Assess for malaria.
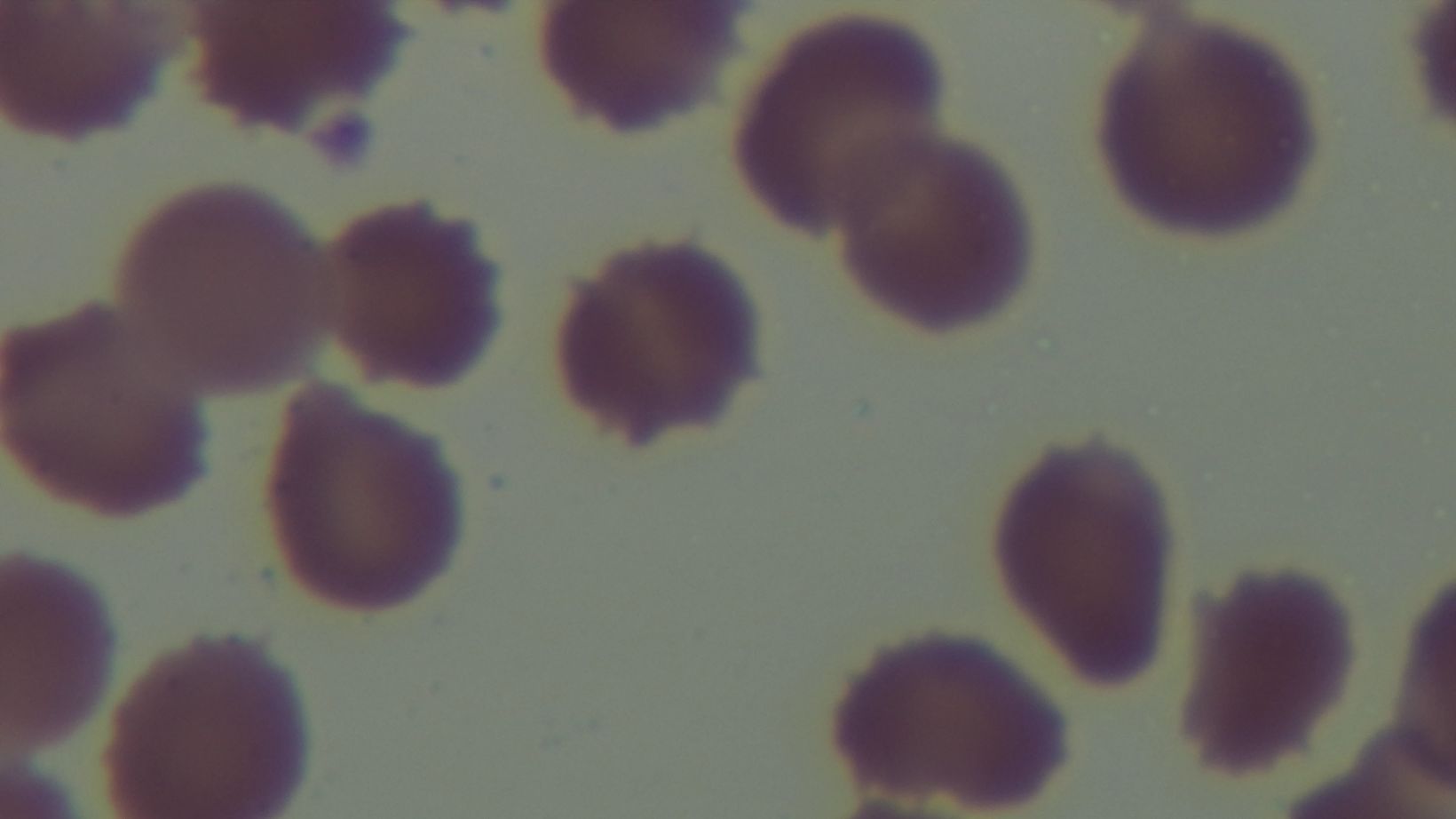
Negative.

100x oil-immersion objective. Photomicrograph. Mounted 4K digital camera. Single field of view. Preparation: thin. Giemsa-stained.